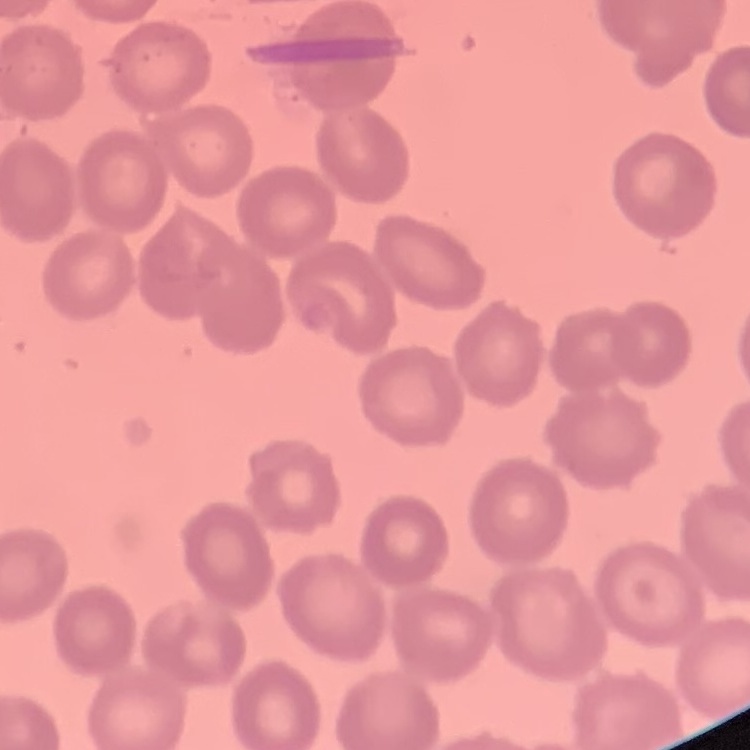

The red blood cells show no rouleaux formation. Thin blood film. Field's or Giemsa stain. One tile cut from a larger photomicrograph.